Locate every blood parasite and identify its species.
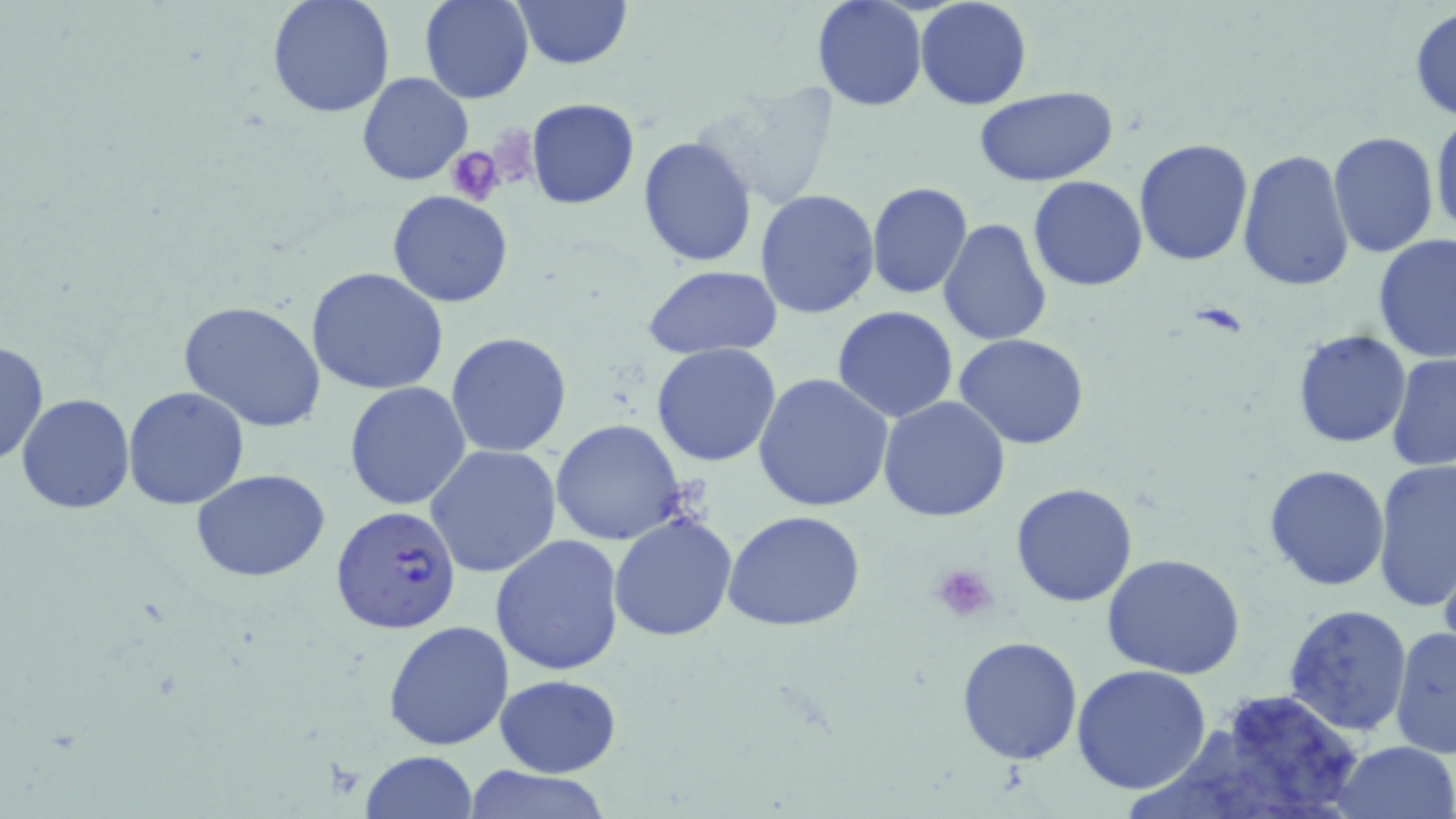

Approximate bounding boxes as named x1/y1/x2/y2 corners in pixels.
Plasmodium falciparum-infected red blood cells: (x1=329, y1=503, x2=463, y2=637).
No Plasmodium ovale, Plasmodium malariae, Plasmodium vivax, Babesia divergens, or Trypanosoma brucei observed.

Uninfected red blood cell locations: (x1=265, y1=0, x2=396, y2=120), (x1=421, y1=0, x2=533, y2=104), (x1=510, y1=0, x2=633, y2=70), (x1=812, y1=0, x2=926, y2=113), (x1=915, y1=0, x2=1032, y2=110), (x1=1408, y1=6, x2=1456, y2=123), (x1=356, y1=72, x2=473, y2=186), (x1=694, y1=81, x2=842, y2=210), (x1=973, y1=86, x2=1120, y2=186), (x1=525, y1=97, x2=641, y2=209), (x1=1431, y1=109, x2=1456, y2=241), (x1=1328, y1=131, x2=1439, y2=257), (x1=638, y1=134, x2=759, y2=268), (x1=1133, y1=138, x2=1252, y2=266), (x1=1238, y1=148, x2=1357, y2=293), (x1=1025, y1=154, x2=1251, y2=275), (x1=1027, y1=176, x2=1149, y2=291), (x1=866, y1=182, x2=973, y2=300), (x1=387, y1=190, x2=515, y2=309), (x1=754, y1=190, x2=882, y2=320), (x1=937, y1=217, x2=1053, y2=345), (x1=1372, y1=234, x2=1456, y2=363), (x1=643, y1=265, x2=785, y2=360), (x1=306, y1=266, x2=449, y2=395), (x1=179, y1=300, x2=330, y2=434), (x1=833, y1=305, x2=961, y2=423), (x1=1292, y1=330, x2=1412, y2=447), (x1=446, y1=332, x2=573, y2=459), (x1=953, y1=332, x2=1090, y2=450), (x1=0, y1=339, x2=49, y2=467), (x1=651, y1=344, x2=781, y2=467), (x1=1386, y1=353, x2=1456, y2=473), (x1=753, y1=372, x2=893, y2=512), (x1=345, y1=382, x2=473, y2=510), (x1=122, y1=387, x2=249, y2=511), (x1=17, y1=394, x2=135, y2=514), (x1=877, y1=396, x2=1011, y2=522), (x1=550, y1=420, x2=687, y2=544), (x1=425, y1=444, x2=564, y2=579), (x1=1374, y1=458, x2=1456, y2=614), (x1=1264, y1=464, x2=1391, y2=591), (x1=190, y1=468, x2=333, y2=582), (x1=1012, y1=482, x2=1140, y2=608), (x1=722, y1=509, x2=867, y2=631), (x1=610, y1=512, x2=740, y2=643), (x1=490, y1=534, x2=626, y2=676), (x1=1437, y1=550, x2=1456, y2=664), (x1=1101, y1=553, x2=1248, y2=680), (x1=1282, y1=602, x2=1413, y2=739), (x1=385, y1=621, x2=515, y2=751), (x1=1390, y1=625, x2=1456, y2=762), (x1=956, y1=636, x2=1083, y2=765), (x1=1071, y1=665, x2=1212, y2=796), (x1=494, y1=674, x2=620, y2=777), (x1=1195, y1=687, x2=1367, y2=818), (x1=1330, y1=740, x2=1456, y2=819), (x1=360, y1=750, x2=479, y2=819), (x1=456, y1=766, x2=615, y2=819). Platelet locations: (x1=446, y1=145, x2=508, y2=204), (x1=930, y1=561, x2=1001, y2=623). Slide-level diagnosis: Plasmodium falciparum. 1000x magnification. Image is 1456×819 pixels. Light microscopy. May-Grünwald-Giemsa-stained preparation. Thin blood film. Single field of view.